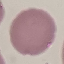
Malaria status: uninfected. Cell patch, automatically extracted from a larger field of view and resized to 64 × 64 pixels. Giemsa-stained preparation. Acquired by smartphone through the microscope eyepiece. Thin blood smear.